State which parasite is depicted.
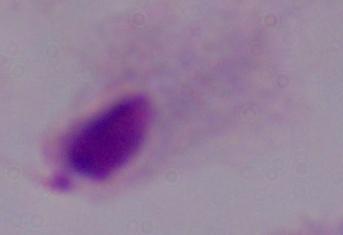
A trichomonad.

Summary:
  - Modality: micrograph
  - Magnification: 1000x